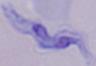
Photomicrograph. Captured at 1000x magnification. A trypanosome is seen.